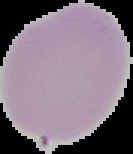

preparation = thin blood smear
image type = segmented cell region on a black background
image size = 133×154 pixels
malaria status = uninfected